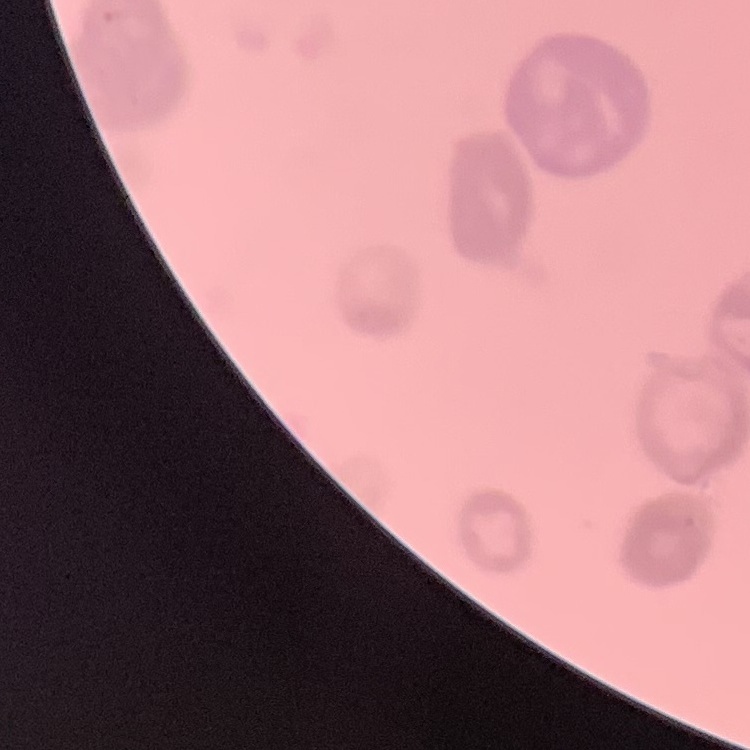

The red blood cells show rouleaux formation. Square crop of a larger photomicrograph. Field's or Giemsa stain. Thin blood film.